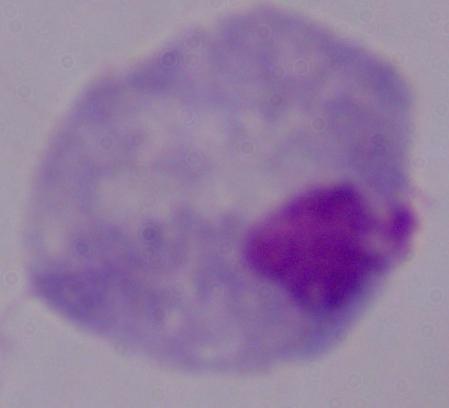

A trichomonad is seen. Photomicrograph. 1000x magnification.